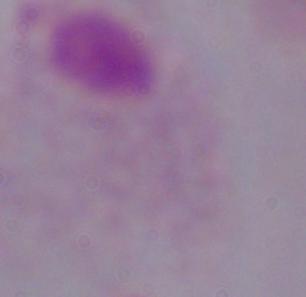

{
  "magnification": "1000x",
  "modality": "photomicrograph",
  "identification": "trichomonad"
}